Name the blood parasite species.
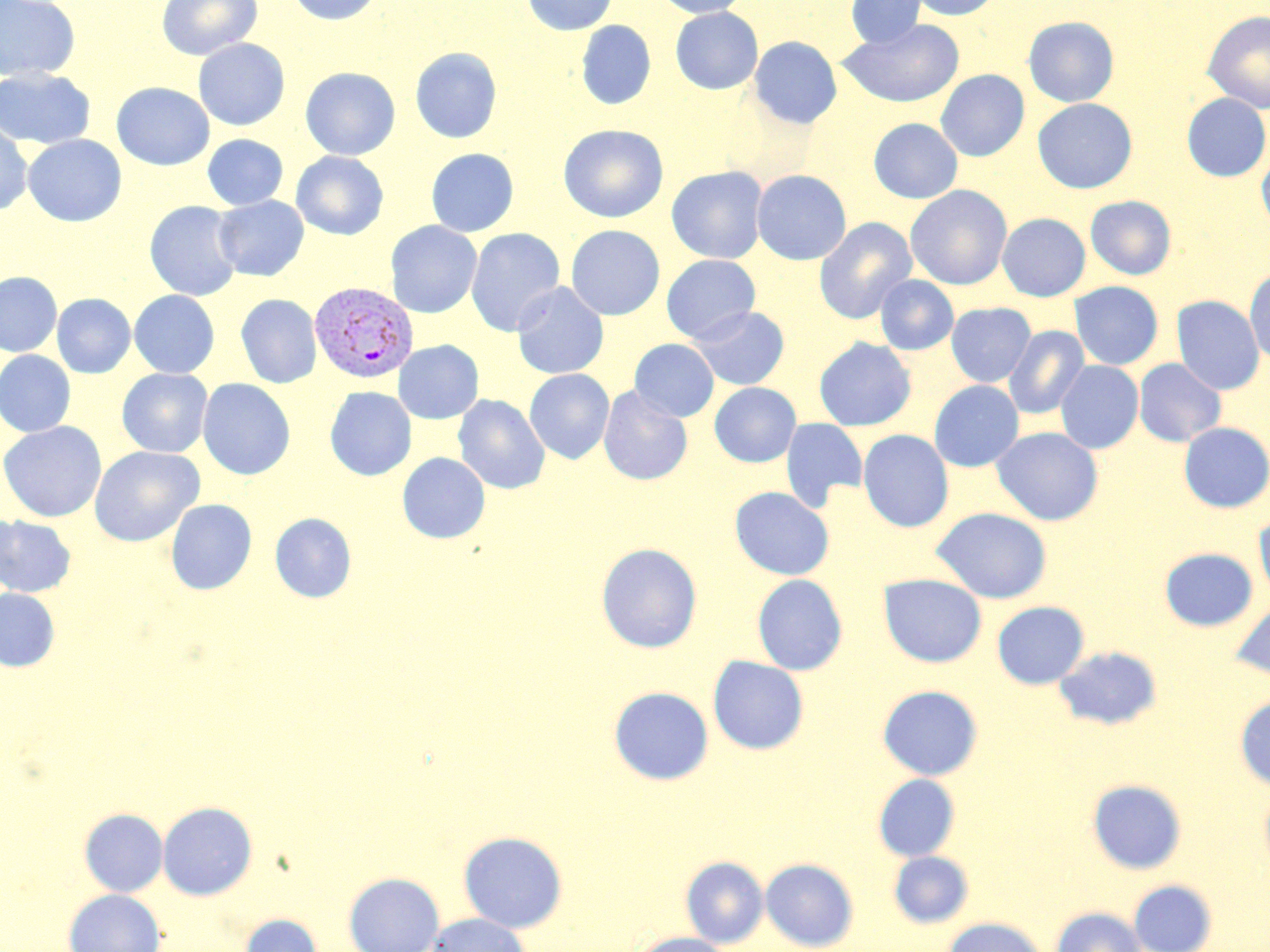

Plasmodium vivax.

Approximate bounding boxes as [x1, y1, x2, y2] in pixels. Plasmodium vivax-infected red blood cell locations: [309, 281, 418, 384]. Uninfected red blood cell locations: [0, 0, 81, 82], [156, 0, 262, 60], [286, 0, 385, 26], [521, 0, 617, 35], [654, 0, 751, 17], [845, 0, 926, 48], [908, 0, 1001, 21], [670, 7, 763, 94], [1202, 11, 1270, 114], [1023, 16, 1119, 107], [841, 19, 964, 108], [576, 20, 656, 110], [749, 36, 842, 128], [193, 38, 291, 131], [410, 47, 502, 143], [300, 67, 401, 160], [0, 68, 95, 149], [935, 69, 1029, 161], [111, 82, 215, 170], [1182, 94, 1270, 182], [1032, 98, 1137, 193], [868, 118, 963, 204], [0, 121, 33, 216], [559, 124, 668, 223], [23, 134, 127, 227], [202, 134, 288, 210], [425, 148, 519, 237], [1257, 150, 1270, 234], [291, 151, 389, 240], [666, 166, 769, 264], [752, 169, 851, 265], [906, 185, 1012, 290], [1085, 195, 1177, 280], [213, 196, 309, 281], [144, 201, 243, 301], [997, 213, 1091, 302], [814, 217, 917, 324], [385, 221, 482, 318], [565, 225, 665, 320], [465, 227, 566, 336], [662, 255, 760, 344], [1244, 266, 1270, 366], [0, 271, 62, 357], [875, 275, 959, 355], [1069, 281, 1163, 370], [511, 282, 609, 379], [129, 290, 220, 378], [52, 293, 136, 378], [129, 293, 324, 379], [235, 294, 322, 389], [1171, 296, 1265, 395], [946, 302, 1036, 387], [689, 306, 790, 390], [1004, 326, 1090, 420], [814, 337, 916, 431], [629, 339, 719, 422], [393, 340, 484, 424], [0, 350, 76, 437], [1134, 358, 1226, 447], [1056, 361, 1143, 454], [117, 368, 213, 457], [524, 369, 615, 464], [197, 378, 296, 480], [929, 380, 1024, 472], [710, 382, 801, 467], [598, 385, 693, 485], [324, 386, 416, 480], [453, 394, 550, 495], [780, 418, 868, 512], [0, 421, 107, 522], [1179, 422, 1270, 512], [991, 427, 1104, 526], [858, 429, 954, 532], [89, 445, 204, 547], [397, 452, 490, 543], [730, 486, 834, 580], [165, 499, 257, 595], [931, 507, 1052, 604], [270, 513, 357, 602], [1254, 514, 1270, 601], [0, 515, 77, 598], [596, 542, 703, 653], [1159, 548, 1258, 631], [878, 573, 987, 667], [752, 574, 848, 675], [0, 588, 60, 671], [992, 601, 1089, 689], [1230, 601, 1270, 681], [1054, 645, 1162, 730], [707, 656, 809, 755], [877, 685, 983, 780], [609, 686, 714, 785], [1234, 695, 1270, 791], [873, 773, 960, 861], [1087, 779, 1187, 875], [1259, 784, 1270, 875], [158, 801, 258, 900], [79, 808, 168, 897], [458, 831, 568, 933], [888, 850, 974, 928], [681, 856, 768, 947], [760, 858, 859, 951], [343, 872, 444, 952], [1128, 879, 1218, 952], [64, 889, 165, 952], [1050, 906, 1147, 952], [237, 913, 323, 952], [426, 913, 529, 952], [941, 917, 1047, 952], [630, 932, 731, 952]. May-Grünwald-Giemsa-stained preparation. Image is 1270×952 pixels. Captured at 1000x magnification. Thin blood film. Single field of view. Light microscopy.